Classify this cell by malaria status.
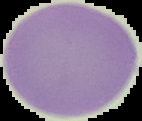

It is uninfected.

Image is 142×121 pixels. From a thin blood smear. Cell region segmented out of the field of view; the surrounding area is masked to black.